Give the position of every leukocyte visible.
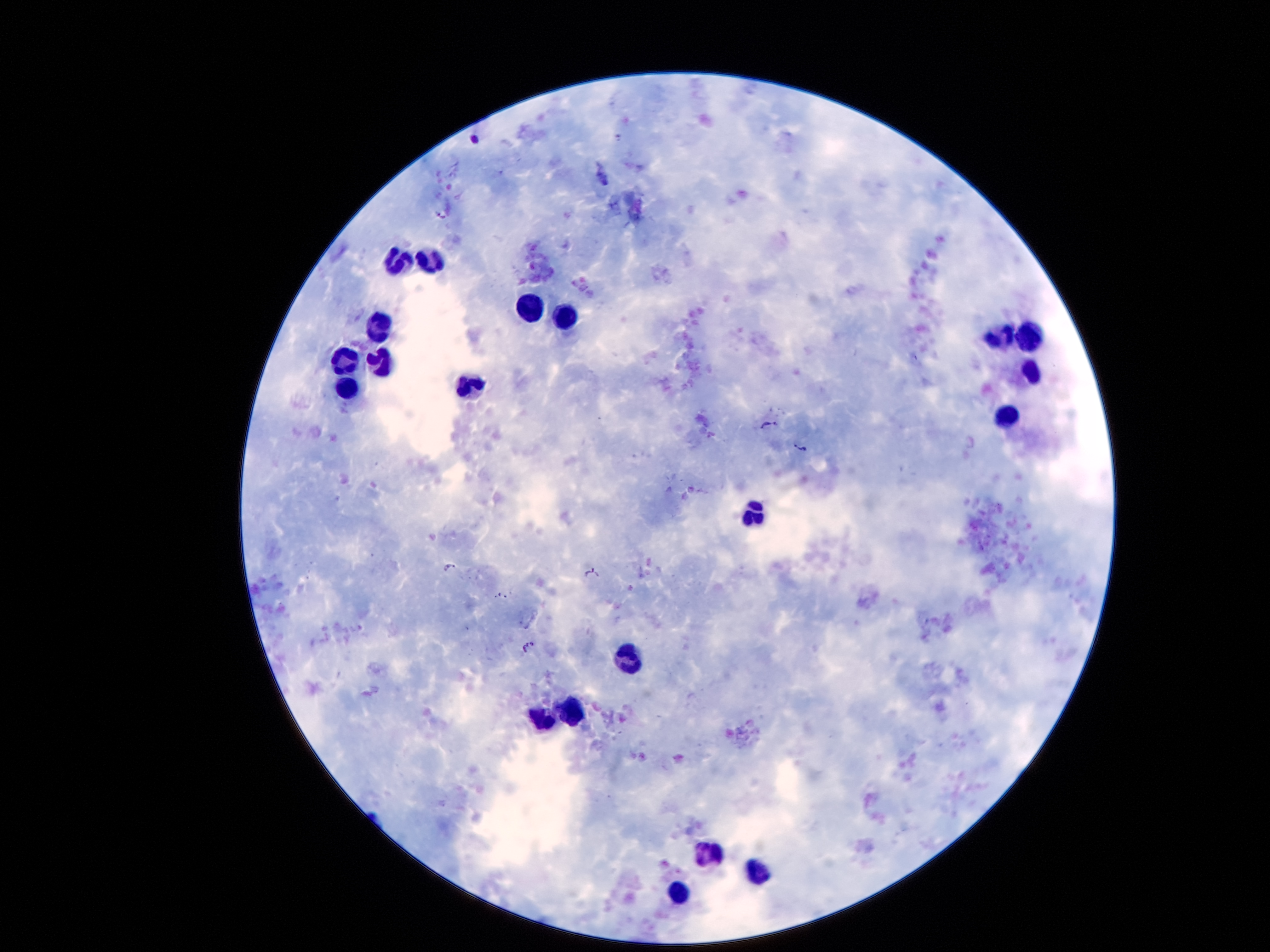

Approximate centers as {x, y} in pixels.
Leukocytes: {431, 262}, {400, 265}, {532, 311}, {565, 315}, {381, 327}, {1029, 333}, {996, 336}, {348, 359}, {381, 360}, {1033, 375}, {471, 388}, {347, 390}, {1011, 415}, {760, 516}, {630, 659}, {573, 707}, {545, 720}, {709, 856}, {753, 874}, {682, 890}.

{
  "patient_malaria_status": "positive for Plasmodium falciparum",
  "capture": "smartphone camera through the microscope eyepiece",
  "stain": "Giemsa",
  "malaria_parasite_locations": "approximate centers as {x, y} in pixels: {473, 139}, {441, 214}, {766, 425}, {802, 447}, {451, 567}, {592, 573}, {528, 646}",
  "field_of_view": "single",
  "image_size": "1270×952 pixels",
  "preparation": "thick peripheral-blood smear",
  "magnification": "100x"
}